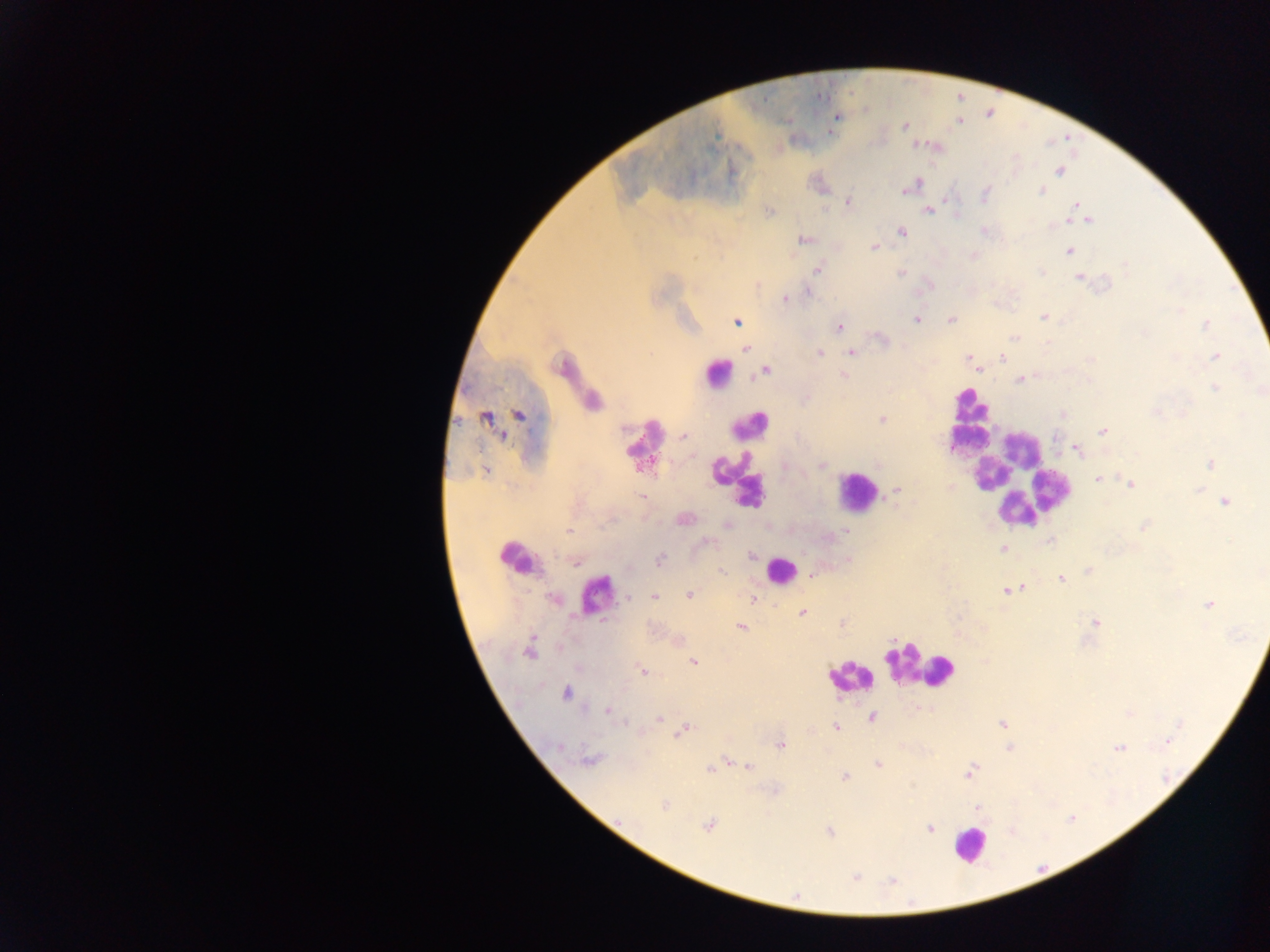 Approximate centers as {x, y} in pixels. Leukocyte locations: {715, 377}, {969, 404}, {750, 424}, {968, 439}, {646, 447}, {730, 463}, {1012, 474}, {856, 492}, {748, 495}, {521, 558}, {779, 569}, {598, 598}, {917, 665}, {850, 677}, {970, 845}. Malaria parasite locations: {836, 117}, {905, 126}, {1059, 171}, {910, 186}, {1042, 190}, {985, 194}, {848, 203}, {1076, 204}, {928, 210}, {769, 212}, {1088, 220}, {984, 230}, {902, 232}, {804, 240}, {874, 247}, {1069, 251}, {819, 269}, {901, 272}, {1041, 272}, {1079, 278}, {808, 292}, {786, 300}, {1044, 317}, {917, 319}, {951, 320}, {736, 322}, {1205, 325}, {840, 326}, {1014, 337}, {881, 339}, {746, 350}, {819, 353}, {852, 353}, {969, 357}, {1216, 357}, {1003, 358}, {1090, 359}, {765, 371}, {844, 376}, {1020, 380}, {1214, 388}, {1155, 412}, {520, 414}, {1062, 414}, {486, 419}, {882, 419}, {1103, 432}, {683, 436}, {1078, 451}, {1211, 463}, {822, 466}, {486, 472}, {1098, 479}, {1130, 484}, {896, 491}, {641, 497}, {1225, 501}, {684, 519}, {728, 525}, {1144, 526}, {568, 531}, {845, 531}, {1050, 541}, {707, 542}, {1002, 548}, {751, 555}, {660, 559}, {576, 563}, {722, 571}, {1089, 572}, {811, 576}, {1061, 579}, {1009, 589}, {689, 594}, {654, 596}, {629, 597}, {752, 600}, {1210, 605}, {803, 612}, {1095, 622}, {741, 627}, {528, 651}, {693, 661}, {642, 671}, {567, 693}, {608, 712}, {873, 718}, {659, 720}, {1002, 724}, {836, 727}, {684, 731}, {1169, 740}, {781, 745}, {559, 747}, {1119, 748}, {1009, 749}, {590, 760}, {878, 764}, {749, 767}, {711, 769}, {969, 772}, {844, 777}, {665, 804}, {978, 808}, {709, 826}, {929, 828}, {829, 832}, {855, 877}, {892, 880}. Image is 1270×952 pixels. Thick blood film. Collected in Ghana. Photographed through a microscope with a mobile-phone camera. One field of view.